Comment on the morphology of the red blood cells.
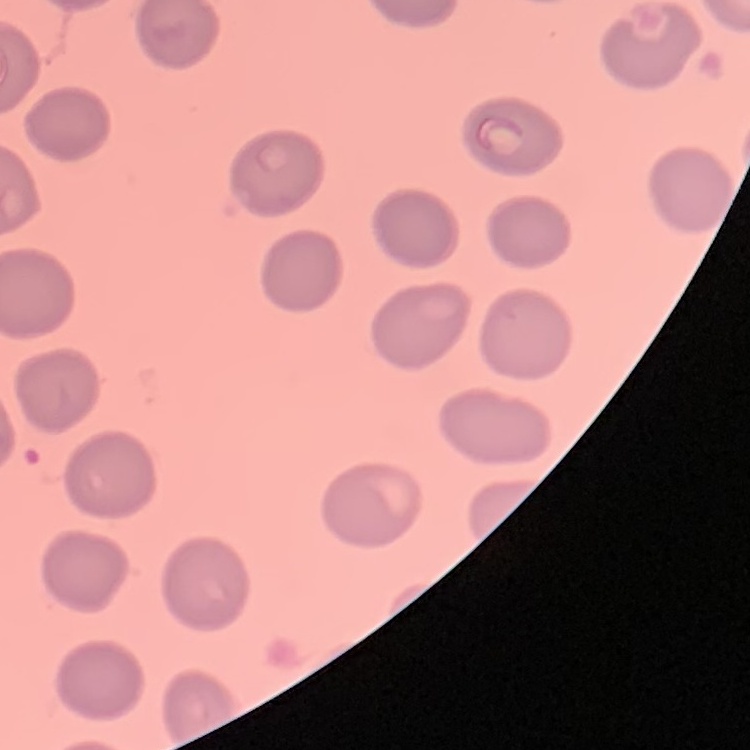
They show no rouleaux formation.

Summary:
  - Stain: Field's or Giemsa
  - Image type: square crop of a larger photomicrograph
  - Preparation: thin blood film